Outline every Plasmodium parasite, every leukocyte, and every artifact (stain precipitate or debris).
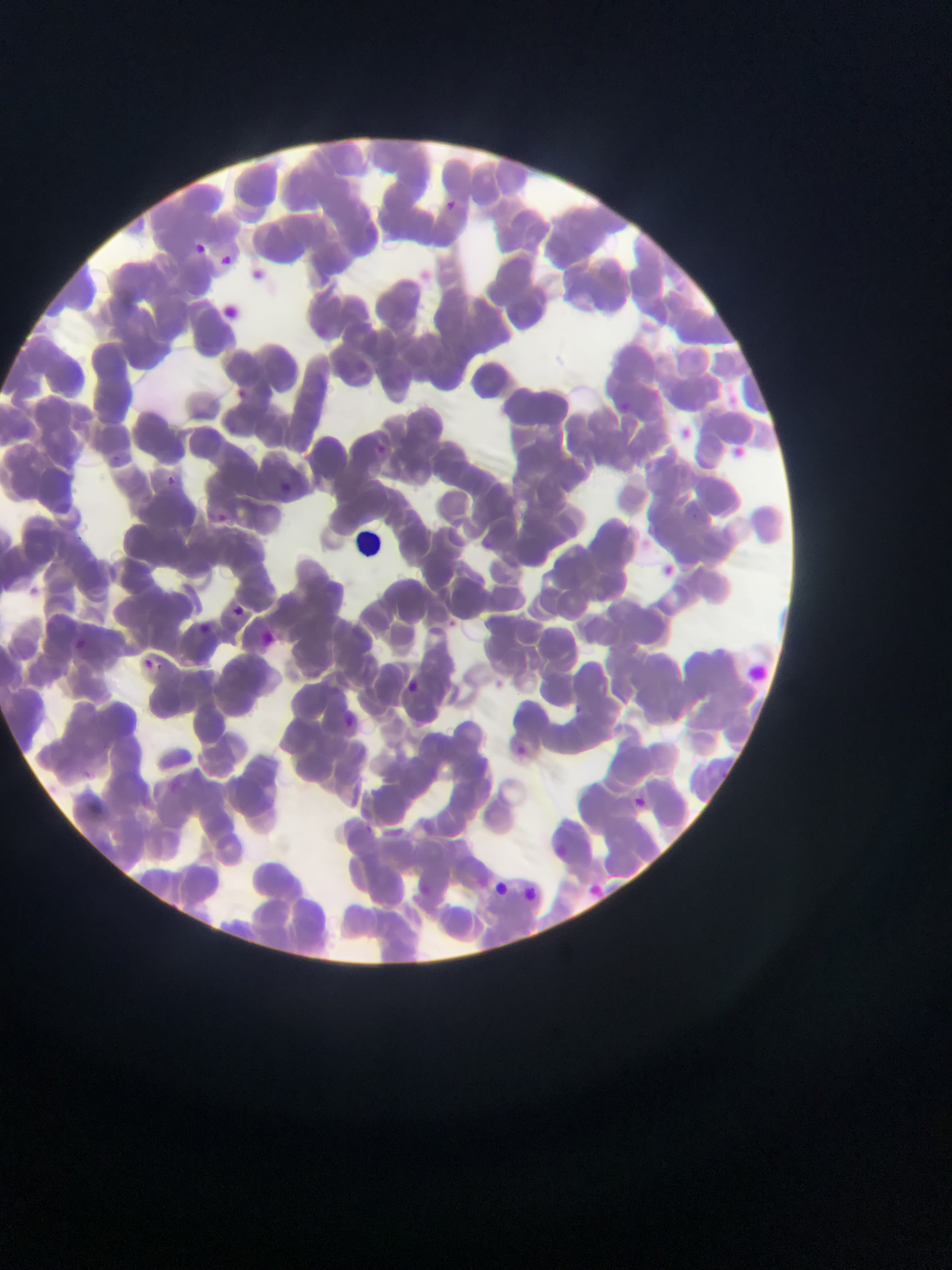

Approximate bounding boxes as left top right bottom in pixels.
Plasmodium parasites: 446 196 462 214; 192 235 204 252; 218 251 239 272; 250 266 267 280; 236 381 257 404; 644 384 674 409; 619 399 634 417; 678 421 695 433; 376 438 390 453; 731 443 753 465; 166 476 176 485; 281 479 298 492; 209 510 232 527; 660 561 685 580; 234 606 245 619; 442 616 458 627; 195 618 212 634; 256 630 275 645; 68 632 83 645; 141 655 158 667; 408 676 420 689; 344 705 355 723; 512 736 547 767; 626 791 650 805; 537 839 573 869; 489 873 520 899; 570 877 604 906; 523 882 539 900.
Leukocytes: 354 523 389 576.

country = Ghana
field of view = single
capture = mobile-phone photograph through a microscope
preparation = thin blood smear
image size = 952×1270 pixels